Report the malaria status of this cell.
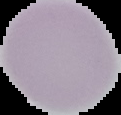

Uninfected.

image size = 121×115 pixels
preparation = thin blood smear
image type = cell region segmented out of the field of view; surrounding area masked to black